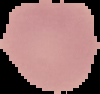
Summary:
  - Preparation: thin blood film
  - Image type: segmented cell region on a black background
  - Image size: 100×94 pixels
  - Result: no malaria parasites detected